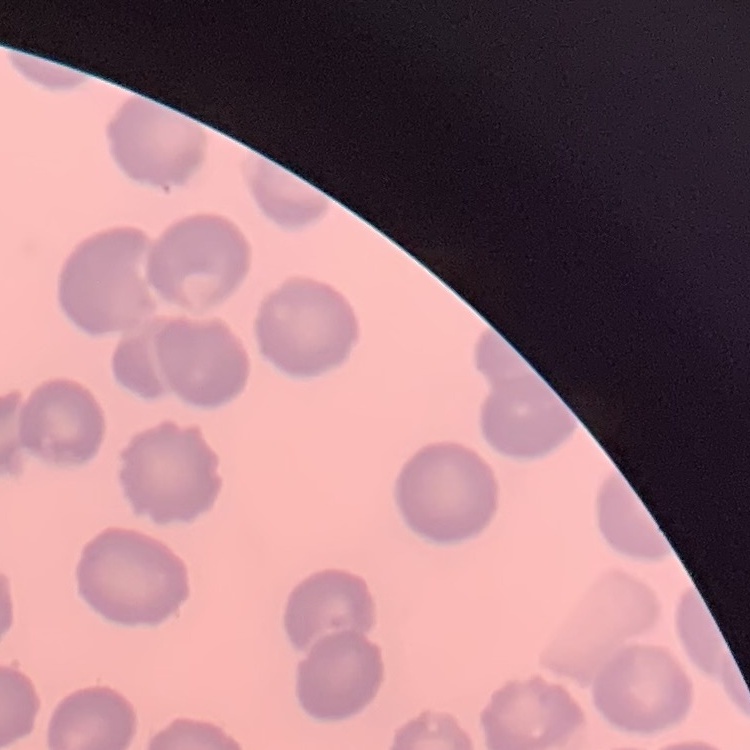

Summary:
  - Erythrocyte morphology: no rouleaux formation
  - Stain: Field's or Giemsa
  - Image type: one tile cut from a larger photomicrograph
  - Preparation: thin blood smear